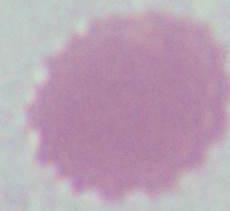

{
  "modality": "photomicrograph",
  "magnification": "1000x",
  "identification": "erythrocyte"
}